Report the malaria status of this cell.
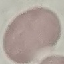
It is uninfected.

Automatically extracted cell patch, resized to 64 × 64 pixels. Giemsa-stained preparation. Acquired by smartphone through the microscope eyepiece. Thin blood smear.